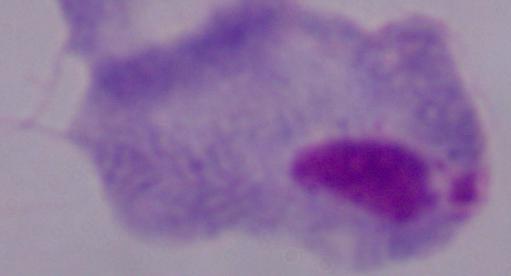
identification = trichomonad
modality = photomicrograph
magnification = 1000x